Report the malaria status of this cell.
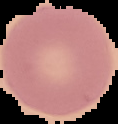

Uninfected.

Image is 118×124 pixels. Cell region segmented out of the field of view; the surrounding area is masked to black. From a thin blood film.